Comment on the morphology of the erythrocytes.
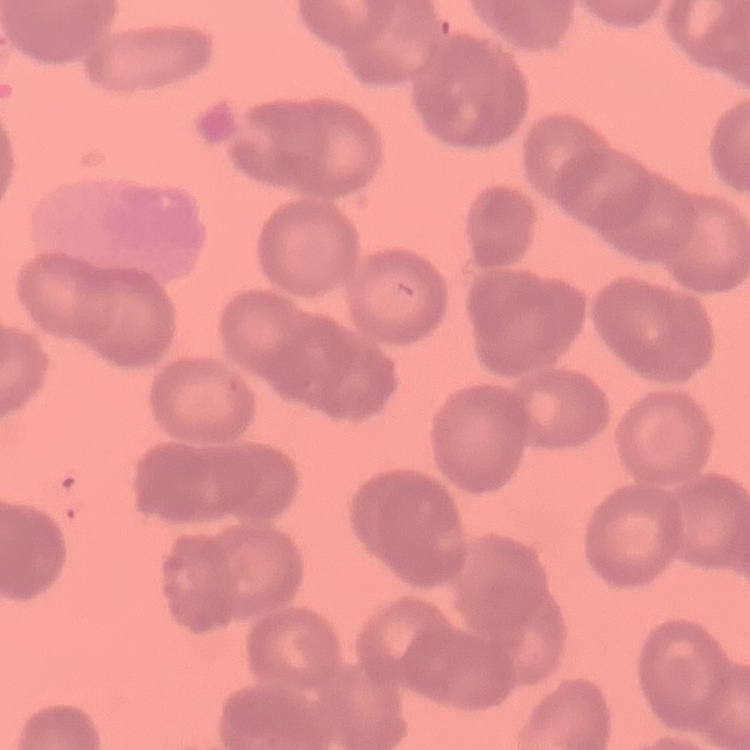
Rouleaux formation.

image type = square crop of a larger photomicrograph
stain = Field's or Giemsa
preparation = thin peripheral smear